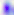

Summary:
  - Identification: Toxoplasma gondii
  - Modality: photomicrograph
  - Magnification: 400x